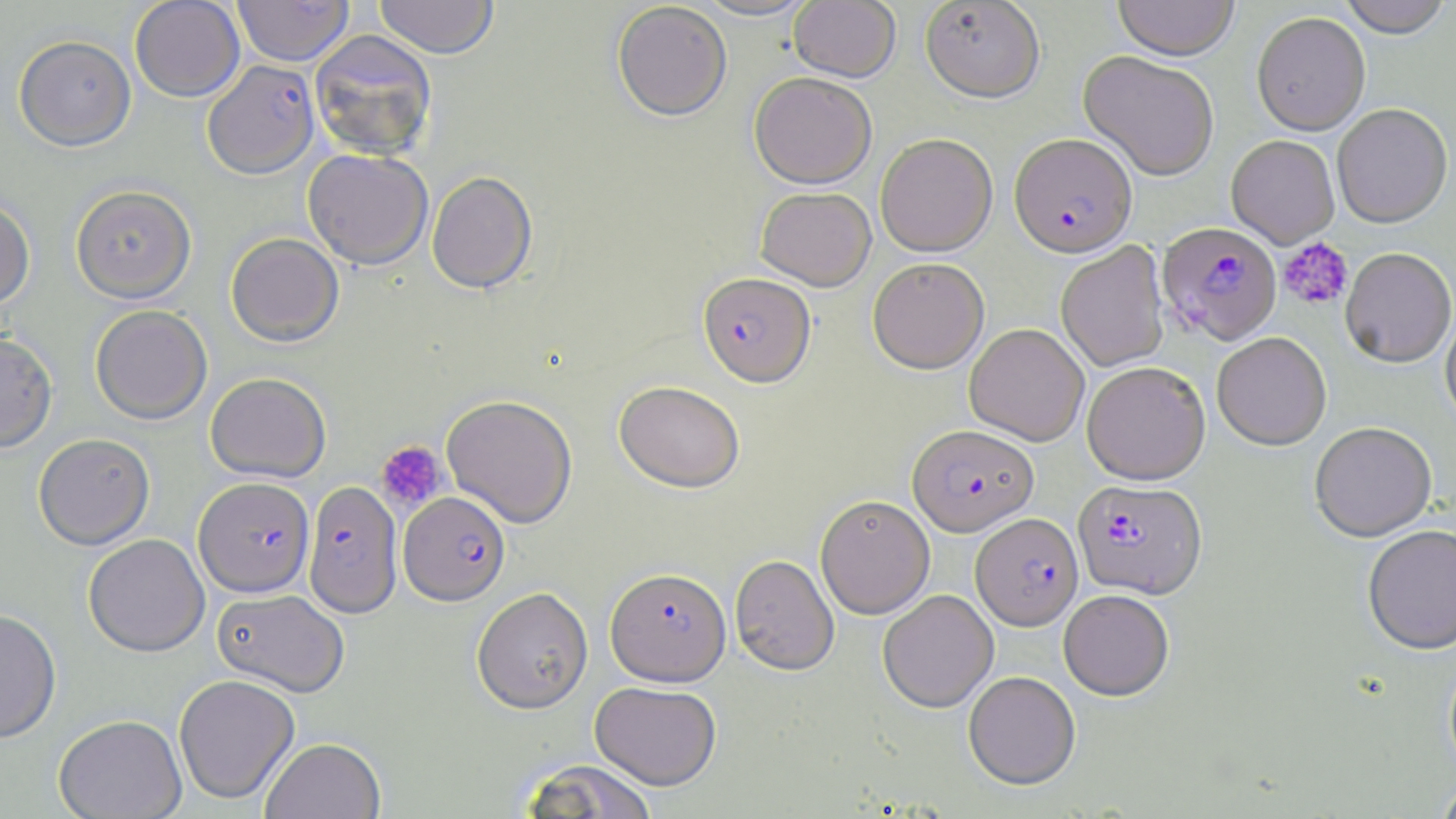
Summary:
  - Coordinate format: approximate bounding boxes as (x1,y1)-(x2,y2) corner pairs in pixels
  - Platelet locations: (1279,237)-(1353,310), (376,440)-(447,512)
  - Plasmodium falciparum-infected red blood cell locations: (203,59)-(319,179), (1009,134)-(1137,258), (1156,223)-(1282,346), (698,272)-(815,387), (908,425)-(1038,537), (193,476)-(315,597), (1072,480)-(1208,600), (302,482)-(401,619), (399,491)-(510,605), (971,513)-(1083,631), (605,567)-(731,686)
  - Uninfected red blood cell locations: (129,0)-(245,102), (231,0)-(354,66), (374,0)-(498,59), (693,0)-(815,22), (1113,0)-(1239,61), (1338,0)-(1454,38), (789,1)-(901,83), (920,1)-(1044,102), (612,2)-(732,122), (1252,12)-(1370,136), (309,30)-(438,161), (14,34)-(136,151), (1079,50)-(1219,182), (749,73)-(876,190), (1332,104)-(1453,229), (875,134)-(997,257), (1226,135)-(1340,249), (303,149)-(433,269), (426,171)-(538,294), (70,184)-(197,303), (755,187)-(876,291), (0,196)-(36,310), (226,232)-(344,347), (1056,242)-(1170,373), (1339,249)-(1455,369), (867,257)-(989,374), (90,305)-(213,425), (1440,312)-(1456,432), (964,323)-(1089,446), (0,331)-(58,452), (1212,333)-(1331,451), (1082,362)-(1210,485), (205,372)-(331,482), (614,380)-(745,493), (441,394)-(578,528), (1309,424)-(1437,544), (33,432)-(155,549), (815,494)-(935,619), (1362,527)-(1456,658), (83,533)-(210,657), (730,554)-(839,676), (472,586)-(593,713), (212,588)-(350,697), (878,590)-(998,713), (1059,590)-(1174,701), (0,608)-(62,742), (963,671)-(1081,790), (174,673)-(299,804), (590,681)-(721,790), (53,713)-(187,818), (261,736)-(386,819), (519,759)-(658,818), (1435,778)-(1456,819)
  - Slide-level diagnosis: Plasmodium falciparum
  - Preparation: thin blood smear
  - Modality: light microscopy
  - Image size: 1456×819 pixels
  - Field of view: one of a larger specimen
  - Stain: May-Grünwald-Giemsa
  - Magnification: 1000x